Assess for Plasmodium parasites.
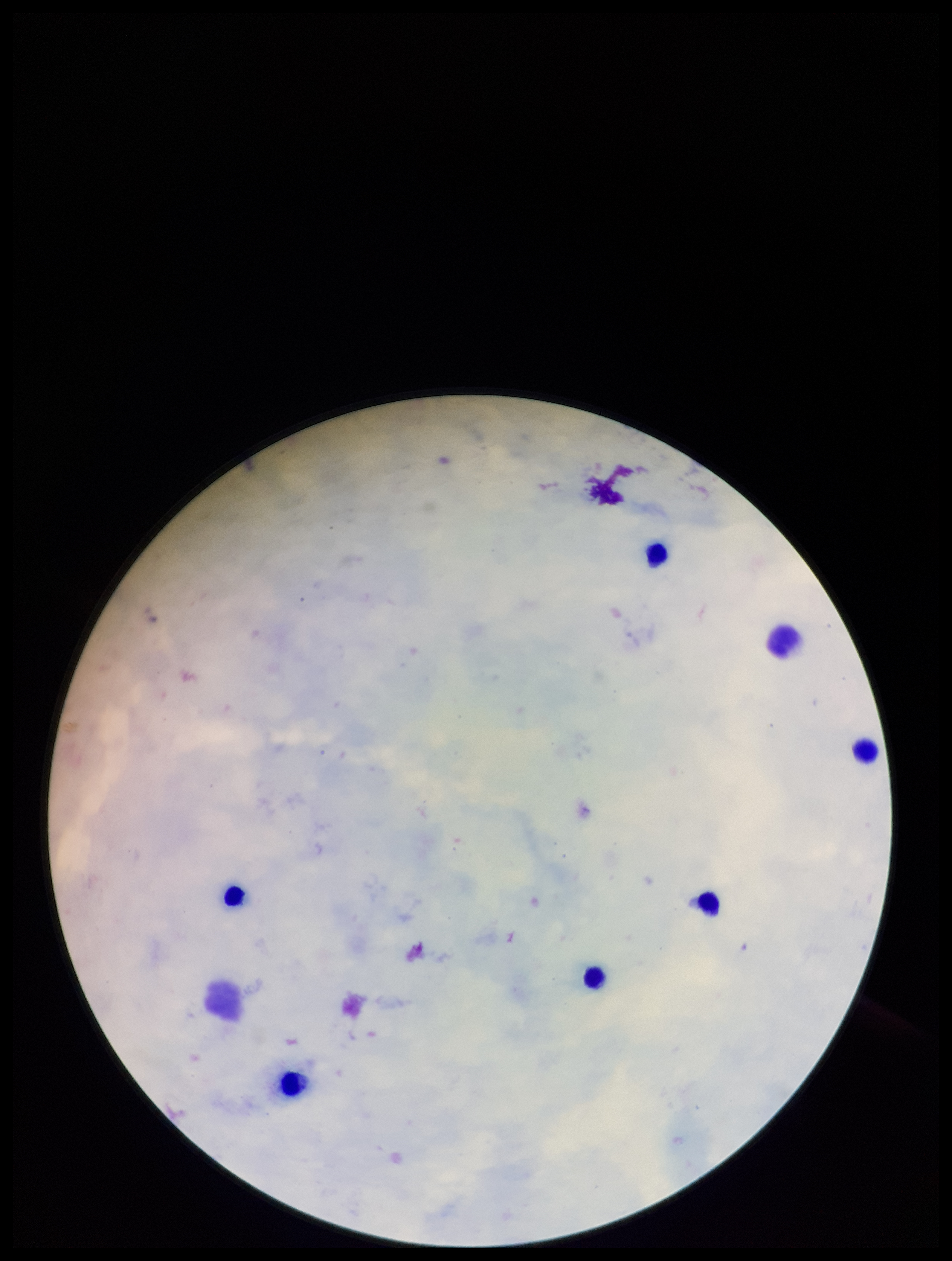
None identified.

Single field of view. Patient malaria status: negative. Parasite count: 0. Leukocyte count: 6. Preparation: thick blood smear. Stained with Giemsa. Photographed through the microscope eyepiece with a smartphone camera. Image is 952×1261 pixels.